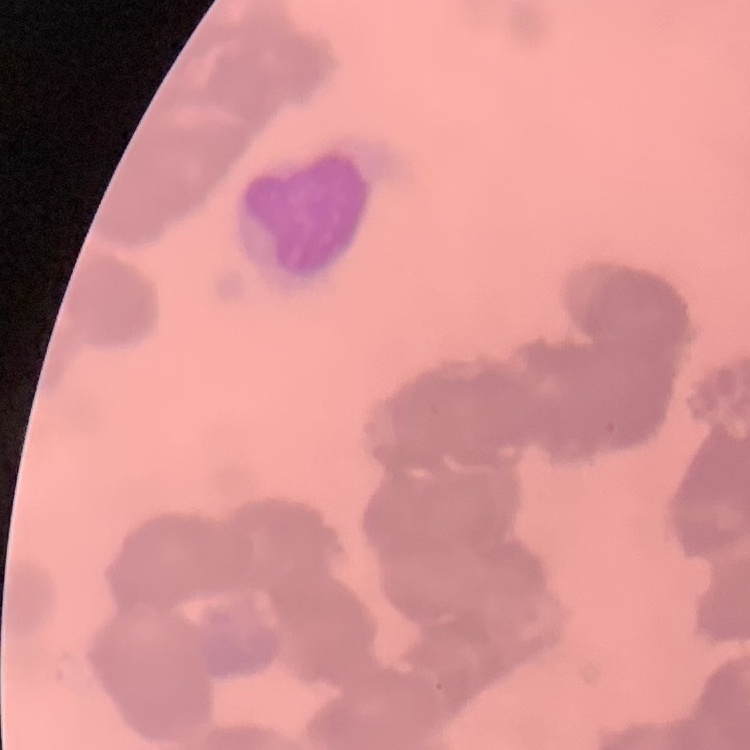

red blood cell morphology = rouleaux formation
image type = square crop of a larger photomicrograph
stain = Field's or Giemsa
preparation = thin peripheral smear